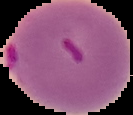

image size = 133×115 pixels
result = malaria parasites identified
image type = cell region segmented out of the field of view; surrounding area masked to black
preparation = thin blood smear